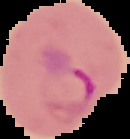
Summary:
  - Malaria status: parasitized
  - Image type: segmented cell region on a black background
  - Preparation: thin blood film
  - Image size: 130×139 pixels